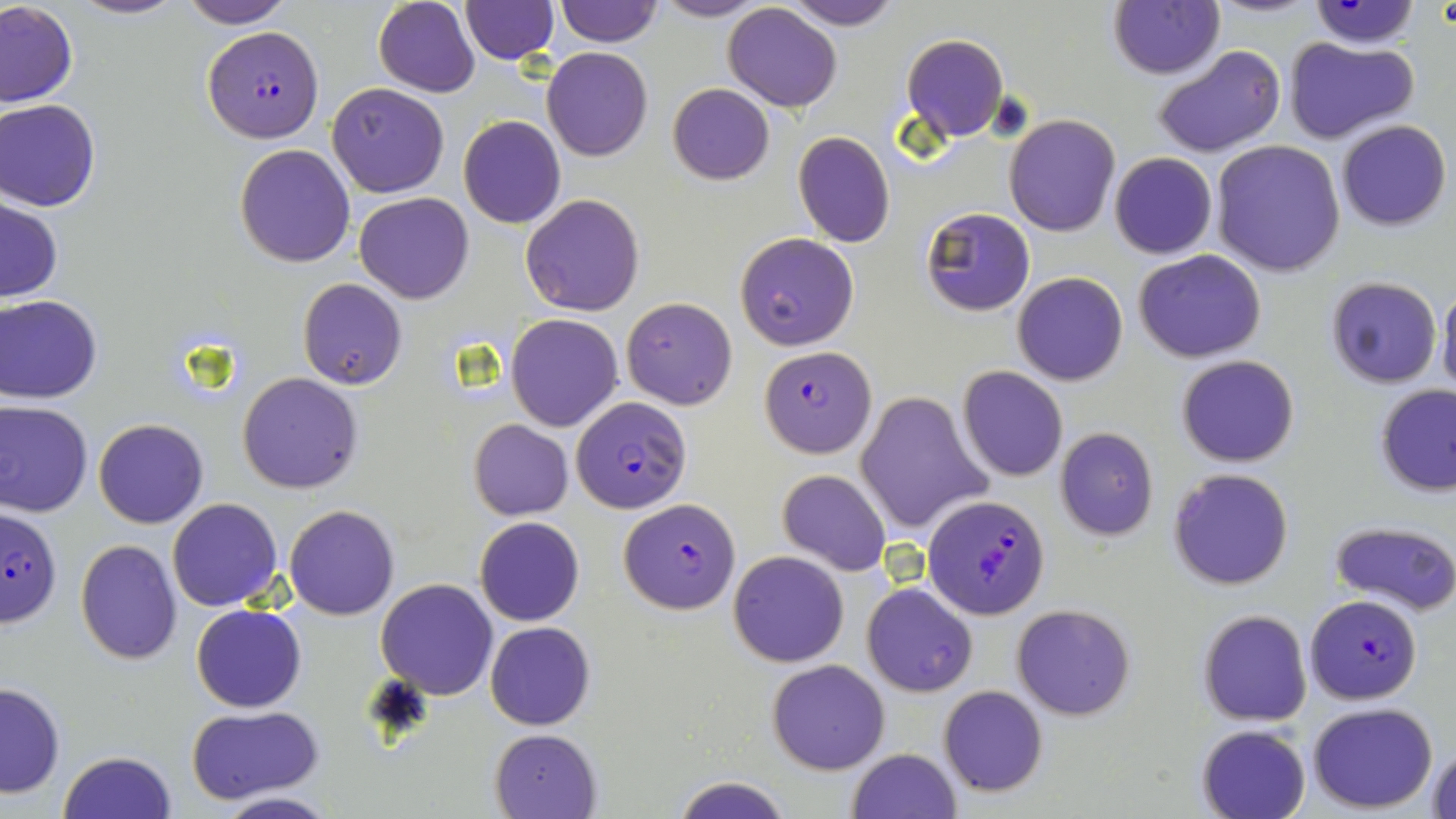
Approximate bounding boxes as named x1/y1/x2/y2 corners in pixels. Plasmodium falciparum-infected red blood cell locations: (x1=202, y1=24, x2=325, y2=143), (x1=759, y1=345, x2=875, y2=456), (x1=571, y1=395, x2=690, y2=512), (x1=923, y1=495, x2=1049, y2=619), (x1=619, y1=499, x2=740, y2=613), (x1=0, y1=507, x2=62, y2=632), (x1=1305, y1=595, x2=1422, y2=704). Uninfected red blood cell locations: (x1=70, y1=0, x2=184, y2=20), (x1=175, y1=0, x2=293, y2=27), (x1=650, y1=0, x2=769, y2=21), (x1=1305, y1=0, x2=1422, y2=49), (x1=373, y1=1, x2=480, y2=97), (x1=460, y1=1, x2=559, y2=62), (x1=552, y1=1, x2=663, y2=48), (x1=783, y1=1, x2=901, y2=30), (x1=0, y1=2, x2=78, y2=108), (x1=1109, y1=2, x2=1224, y2=79), (x1=722, y1=3, x2=843, y2=113), (x1=900, y1=33, x2=1009, y2=143), (x1=1282, y1=36, x2=1418, y2=145), (x1=1153, y1=45, x2=1285, y2=159), (x1=541, y1=47, x2=653, y2=162), (x1=327, y1=83, x2=450, y2=198), (x1=667, y1=84, x2=775, y2=185), (x1=0, y1=99, x2=101, y2=211), (x1=1004, y1=114, x2=1120, y2=237), (x1=458, y1=115, x2=566, y2=229), (x1=1335, y1=119, x2=1451, y2=231), (x1=793, y1=132, x2=894, y2=247), (x1=1210, y1=140, x2=1347, y2=276), (x1=234, y1=143, x2=356, y2=268), (x1=1109, y1=151, x2=1217, y2=260), (x1=353, y1=192, x2=475, y2=304), (x1=520, y1=193, x2=645, y2=316), (x1=1, y1=196, x2=65, y2=305), (x1=920, y1=207, x2=1035, y2=315), (x1=734, y1=232, x2=860, y2=352), (x1=1134, y1=249, x2=1268, y2=363), (x1=1012, y1=272, x2=1127, y2=386), (x1=1324, y1=277, x2=1442, y2=389), (x1=299, y1=279, x2=407, y2=390), (x1=1437, y1=280, x2=1456, y2=399), (x1=0, y1=295, x2=104, y2=404), (x1=622, y1=298, x2=738, y2=410), (x1=505, y1=314, x2=623, y2=431), (x1=1176, y1=354, x2=1300, y2=467), (x1=957, y1=367, x2=1069, y2=482), (x1=237, y1=372, x2=364, y2=494), (x1=1374, y1=384, x2=1456, y2=496), (x1=856, y1=391, x2=992, y2=537), (x1=0, y1=400, x2=94, y2=518), (x1=93, y1=419, x2=208, y2=529), (x1=469, y1=419, x2=574, y2=519), (x1=1054, y1=427, x2=1158, y2=539), (x1=1168, y1=467, x2=1295, y2=592), (x1=777, y1=469, x2=891, y2=575), (x1=166, y1=498, x2=283, y2=612), (x1=284, y1=505, x2=399, y2=619), (x1=474, y1=516, x2=585, y2=627), (x1=1329, y1=519, x2=1456, y2=615), (x1=75, y1=538, x2=183, y2=664), (x1=728, y1=551, x2=850, y2=667), (x1=375, y1=578, x2=499, y2=699), (x1=861, y1=582, x2=978, y2=698), (x1=1011, y1=604, x2=1136, y2=720), (x1=190, y1=605, x2=306, y2=713), (x1=1197, y1=608, x2=1312, y2=726), (x1=485, y1=621, x2=595, y2=730), (x1=767, y1=659, x2=891, y2=774), (x1=0, y1=681, x2=66, y2=798), (x1=939, y1=685, x2=1048, y2=797), (x1=1306, y1=702, x2=1438, y2=812), (x1=184, y1=704, x2=325, y2=805), (x1=1197, y1=724, x2=1311, y2=819), (x1=491, y1=730, x2=600, y2=818), (x1=1426, y1=740, x2=1456, y2=819), (x1=847, y1=748, x2=960, y2=819), (x1=59, y1=750, x2=178, y2=819), (x1=667, y1=776, x2=799, y2=819), (x1=210, y1=791, x2=338, y2=819). Slide-level diagnosis: Plasmodium falciparum. Image is 1456×819 pixels. Captured at 1000x magnification. Optical microscopy. Thin blood smear. May-Grünwald-Giemsa-stained preparation. One field of a larger specimen.